Assess the morphology of the erythrocytes.
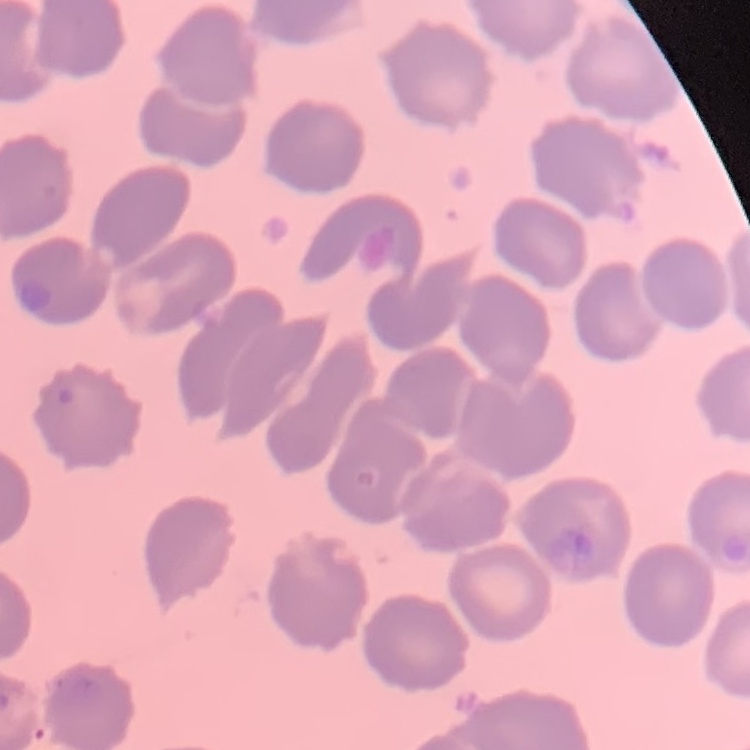

No rouleaux formation.

Summary:
  - Preparation: thin peripheral smear
  - Image type: square crop of a larger photomicrograph
  - Stain: Field's or Giemsa